Outline each blood parasite and name the species.
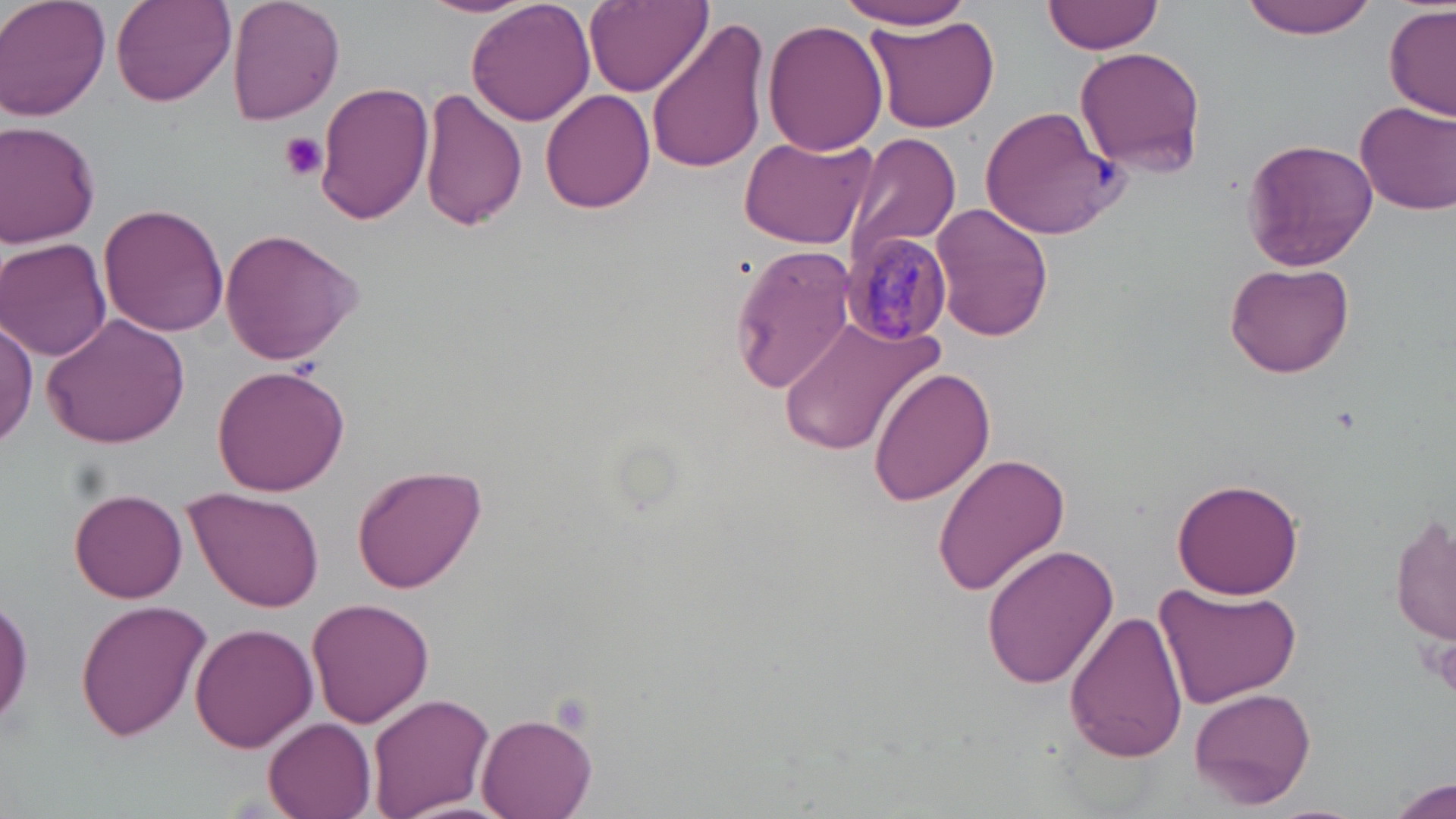

Approximate bounding boxes as (x1,y1)-(x2,y2) corner pairs in pixels.
Plasmodium malariae-infected red blood cells: (844,232)-(953,341).
No Plasmodium falciparum, Plasmodium ovale, Plasmodium vivax, Babesia divergens, or Trypanosoma brucei observed.

Platelet locations: (279,133)-(330,182), (1418,632)-(1456,700). Uninfected red blood cell locations: (1,0)-(111,122), (224,0)-(345,124), (415,0)-(541,19), (833,0)-(981,30), (1043,0)-(1167,55), (1237,0)-(1381,38), (110,1)-(236,108), (466,1)-(595,126), (584,1)-(711,95), (1384,5)-(1456,121), (869,16)-(1000,133), (644,17)-(769,176), (762,20)-(889,157), (1074,46)-(1207,176), (314,80)-(435,225), (417,88)-(526,233), (539,89)-(656,213), (1356,98)-(1456,215), (979,103)-(1121,240), (0,123)-(102,246), (737,131)-(878,250), (842,132)-(964,263), (1241,137)-(1378,271), (100,202)-(230,337), (929,205)-(1054,340), (218,229)-(366,363), (0,237)-(112,362), (728,243)-(860,392), (1224,262)-(1355,379), (780,309)-(943,462), (42,311)-(192,449), (1,314)-(38,452), (211,366)-(351,498), (869,366)-(995,507), (932,452)-(1073,596), (352,466)-(487,591), (1171,478)-(1305,600), (186,487)-(325,612), (70,488)-(188,603), (1390,511)-(1454,648), (980,543)-(1119,691), (1153,582)-(1301,708), (308,597)-(435,727), (74,600)-(213,742), (1065,607)-(1188,765), (192,622)-(317,754), (1189,685)-(1314,809), (367,693)-(496,819), (478,711)-(598,818), (265,717)-(377,819), (1385,776)-(1455,819). Slide-level diagnosis: Plasmodium malariae. Thin blood smear. May-Grünwald-Giemsa-stained preparation. Single field of view. Light microscopy. Captured at 1000x magnification. Image is 1456×819 pixels.